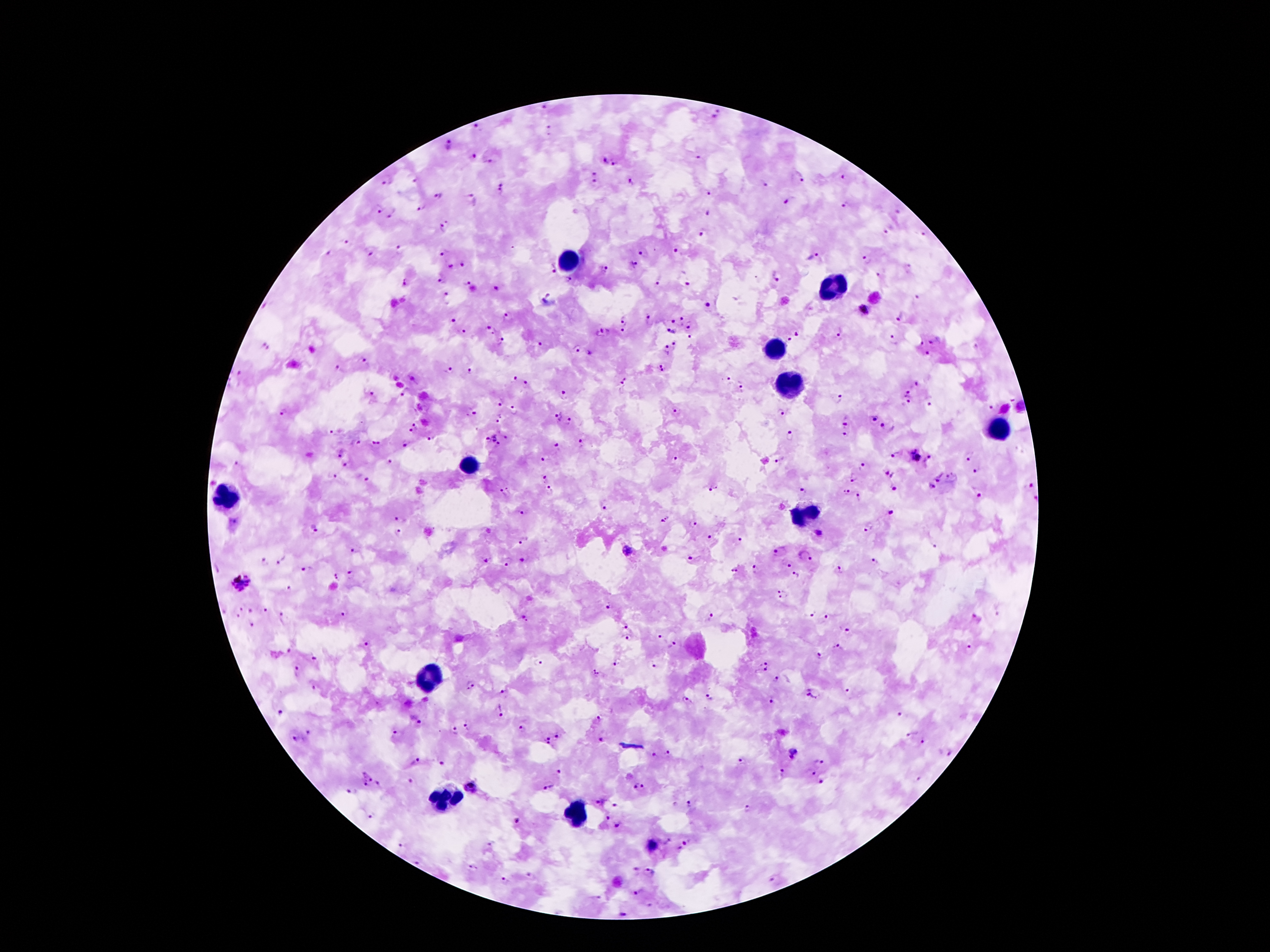

{
  "preparation": "thick blood smear",
  "magnification": "100x",
  "field_of_view": "one from this slide",
  "plasmodium_parasite_locations": "approximate centers as {x, y} in pixels: {545, 106}, {717, 116}, {477, 129}, {551, 131}, {448, 143}, {473, 155}, {699, 157}, {606, 161}, {488, 162}, {614, 165}, {595, 172}, {798, 177}, {843, 177}, {417, 179}, {388, 180}, {595, 182}, {630, 183}, {766, 186}, {502, 189}, {708, 193}, {440, 196}, {472, 200}, {786, 203}, {422, 207}, {845, 207}, {379, 208}, {393, 214}, {708, 214}, {445, 225}, {887, 230}, {703, 234}, {923, 234}, {348, 243}, {674, 248}, {400, 250}, {330, 252}, {369, 252}, {443, 252}, {641, 252}, {813, 257}, {867, 259}, {632, 264}, {464, 265}, {908, 267}, {451, 268}, {604, 268}, {551, 269}, {778, 274}, {877, 276}, {569, 281}, {658, 281}, {441, 282}, {405, 283}, {688, 284}, {470, 287}, {497, 288}, {548, 295}, {918, 297}, {448, 298}, {708, 307}, {863, 312}, {507, 314}, {624, 317}, {901, 317}, {647, 319}, {680, 319}, {453, 321}, {671, 321}, {689, 324}, {490, 329}, {671, 330}, {465, 331}, {624, 331}, {798, 331}, {602, 333}, {840, 333}, {690, 336}, {893, 338}, {790, 339}, {502, 340}, {931, 342}, {539, 344}, {675, 346}, {266, 348}, {576, 349}, {666, 351}, {927, 353}, {591, 354}, {363, 360}, {449, 368}, {338, 369}, {469, 369}, {663, 369}, {238, 373}, {515, 379}, {727, 379}, {623, 382}, {916, 383}, {527, 385}, {741, 385}, {563, 393}, {908, 393}, {370, 394}, {405, 394}, {838, 399}, {908, 401}, {498, 403}, {929, 404}, {991, 408}, {677, 411}, {470, 412}, {780, 412}, {283, 414}, {558, 415}, {873, 418}, {499, 419}, {846, 420}, {569, 421}, {414, 427}, {887, 428}, {334, 431}, {843, 434}, {506, 437}, {790, 437}, {434, 439}, {491, 441}, {376, 442}, {358, 443}, {581, 444}, {403, 446}, {556, 446}, {344, 453}, {895, 454}, {914, 456}, {968, 456}, {928, 457}, {545, 459}, {675, 459}, {780, 459}, {389, 461}, {238, 464}, {349, 465}, {863, 465}, {976, 471}, {888, 474}, {938, 476}, {337, 477}, {853, 477}, {951, 477}, {547, 479}, {365, 480}, {716, 486}, {931, 486}, {1028, 486}, {802, 489}, {893, 489}, {510, 490}, {550, 490}, {710, 490}, {846, 490}, {500, 493}, {977, 493}, {858, 497}, {604, 506}, {892, 512}, {525, 514}, {397, 518}, {665, 518}, {236, 521}, {692, 524}, {868, 526}, {314, 529}, {398, 533}, {819, 533}, {710, 538}, {740, 539}, {524, 541}, {932, 545}, {627, 550}, {353, 551}, {779, 551}, {805, 557}, {691, 558}, {283, 560}, {523, 560}, {264, 561}, {486, 561}, {873, 561}, {508, 564}, {788, 564}, {306, 569}, {756, 569}, {217, 570}, {735, 570}, {838, 571}, {351, 576}, {795, 576}, {335, 577}, {242, 581}, {290, 587}, {782, 594}, {610, 607}, {240, 609}, {267, 610}, {250, 611}, {343, 613}, {812, 614}, {283, 616}, {237, 617}, {710, 617}, {827, 619}, {977, 619}, {524, 621}, {252, 625}, {628, 627}, {847, 629}, {660, 636}, {626, 638}, {367, 645}, {672, 645}, {840, 649}, {969, 649}, {288, 650}, {314, 658}, {819, 658}, {538, 662}, {766, 662}, {615, 664}, {654, 667}, {296, 669}, {762, 672}, {596, 673}, {775, 679}, {471, 685}, {313, 687}, {846, 691}, {503, 692}, {816, 693}, {709, 697}, {687, 701}, {773, 701}, {502, 710}, {281, 711}, {901, 715}, {599, 719}, {420, 725}, {468, 725}, {455, 731}, {523, 731}, {307, 732}, {395, 733}, {912, 734}, {560, 735}, {601, 739}, {295, 740}, {547, 742}, {923, 742}, {948, 753}, {669, 754}, {795, 754}, {655, 756}, {416, 761}, {442, 762}, {741, 762}, {823, 763}, {557, 771}, {782, 773}, {811, 773}, {372, 780}, {408, 780}, {919, 780}, {821, 781}, {471, 787}, {548, 787}, {640, 787}, {351, 793}, {600, 802}, {690, 804}, {616, 807}, {748, 808}, {372, 817}, {607, 818}, {517, 821}, {616, 827}, {668, 841}, {490, 845}, {400, 846}, {652, 846}, {685, 846}, {417, 862}, {473, 867}, {634, 872}, {650, 873}, {531, 877}, {775, 879}, {505, 881}, {640, 892}, {597, 899}, {649, 905}, {621, 914}",
  "leukocyte_locations": "approximate centers as {x, y} in pixels: {568, 258}, {833, 286}, {779, 347}, {790, 388}, {1001, 427}, {468, 463}, {227, 499}, {802, 513}, {431, 683}, {443, 801}, {577, 813}",
  "capture": "smartphone through the microscope eyepiece",
  "stain": "Giemsa",
  "patient_malaria_status": "infected with Plasmodium falciparum",
  "image_size": "1270×952 pixels"
}